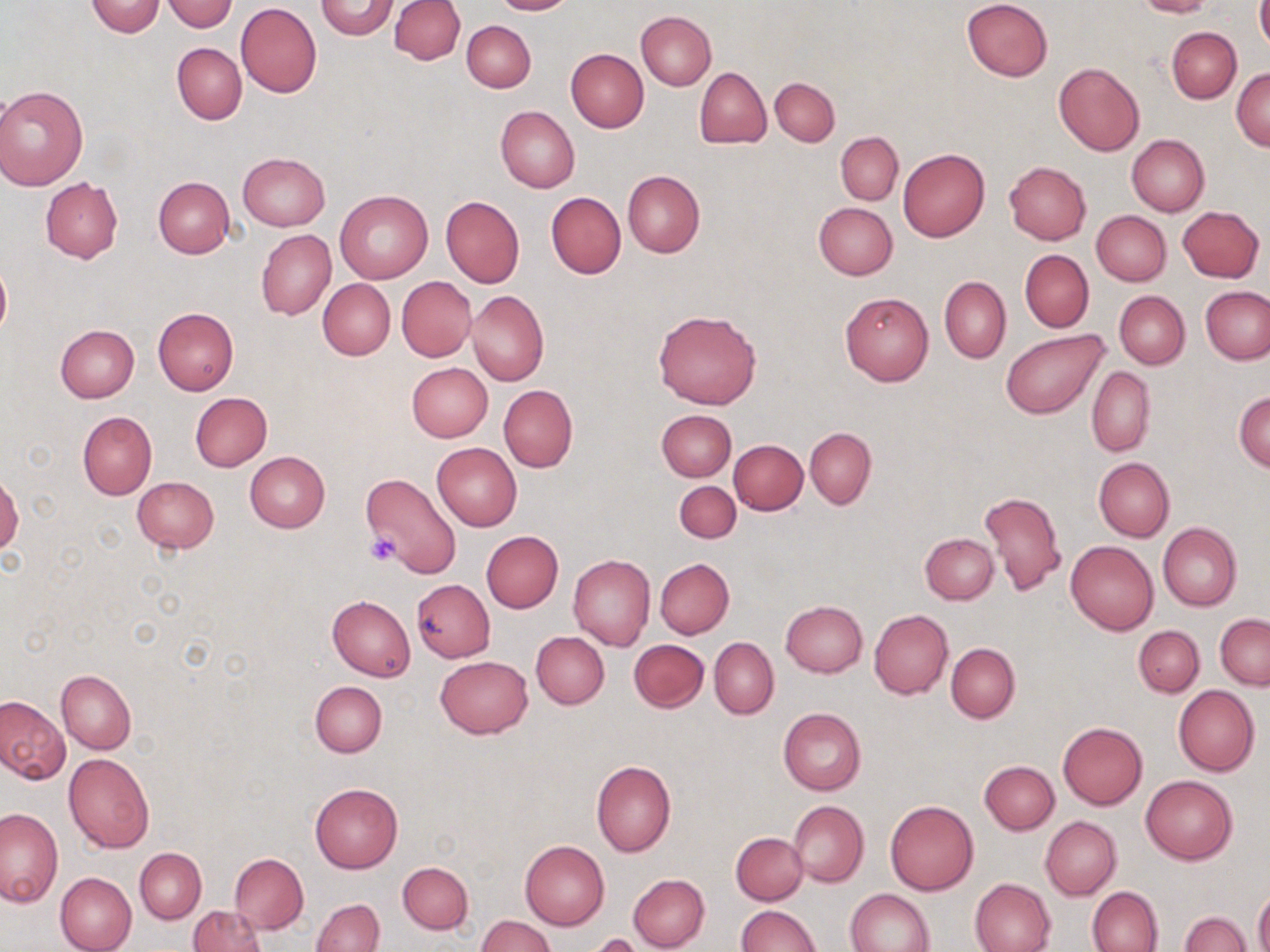

Summary:
  - Coordinate format: approximate bounding boxes as (x1,y1)-(x2,y2) corner pairs in pixels
  - Uninfected red blood cell locations: (84,0)-(166,37), (390,0)-(464,64), (490,0)-(577,15), (961,0)-(1053,82), (1134,0)-(1216,18), (1257,0)-(1270,54), (161,1)-(239,32), (315,1)-(399,39), (236,3)-(322,98), (637,11)-(716,90), (462,20)-(536,92), (1166,27)-(1240,104), (173,43)-(246,124), (565,49)-(649,132), (1053,61)-(1145,155), (1231,66)-(1270,150), (695,68)-(770,148), (769,76)-(839,147), (0,84)-(88,190), (495,106)-(579,193), (836,132)-(903,204), (834,135)-(972,214), (1126,135)-(1210,217), (898,148)-(989,242), (238,153)-(330,230), (1004,161)-(1091,244), (622,170)-(704,258), (154,177)-(235,258), (40,178)-(123,263), (335,189)-(432,283), (545,192)-(626,278), (441,195)-(524,287), (814,203)-(897,280), (1176,206)-(1263,282), (1090,210)-(1171,286), (256,229)-(336,319), (1020,249)-(1093,332), (0,256)-(11,344), (396,276)-(476,363), (940,276)-(1011,363), (318,278)-(395,359), (1200,286)-(1270,365), (466,289)-(549,386), (1114,291)-(1190,369), (839,292)-(934,385), (153,307)-(238,396), (652,309)-(762,410), (54,323)-(139,403), (1000,330)-(1108,419), (406,362)-(492,441), (1086,367)-(1155,456), (499,385)-(576,472), (1234,391)-(1270,471), (190,392)-(272,471), (656,409)-(735,481), (78,411)-(157,500), (805,428)-(876,508), (729,439)-(807,515), (432,442)-(521,531), (244,451)-(330,532), (1093,457)-(1174,542), (362,471)-(462,578), (0,472)-(21,559), (132,476)-(220,553), (675,480)-(741,542), (981,490)-(1067,598), (1157,522)-(1242,611), (482,531)-(563,612), (920,532)-(998,603), (1066,541)-(1158,634), (567,554)-(655,651), (655,559)-(734,638), (412,580)-(495,662), (327,595)-(415,681), (780,600)-(867,677), (869,609)-(953,699), (1216,614)-(1270,690), (1133,626)-(1204,697), (531,631)-(609,709), (709,638)-(778,719), (629,639)-(708,712), (946,642)-(1019,723), (435,655)-(533,738), (57,669)-(136,753), (311,681)-(387,757), (1173,686)-(1259,777), (0,696)-(69,783), (778,708)-(866,795), (1057,722)-(1147,809), (64,752)-(154,853), (591,760)-(676,857), (980,761)-(1059,834), (1141,776)-(1237,864), (310,782)-(403,873), (884,800)-(979,895), (789,801)-(868,887), (0,808)-(63,907), (1041,816)-(1121,901), (731,832)-(808,905), (520,840)-(610,929), (135,848)-(206,922), (230,852)-(308,934), (397,861)-(473,934), (55,872)-(138,952), (628,874)-(710,951), (970,878)-(1056,952), (1088,886)-(1163,952), (845,888)-(934,952), (1254,888)-(1270,952), (311,899)-(384,952), (188,905)-(266,952), (735,905)-(819,952), (1179,911)-(1251,951), (478,914)-(555,952), (585,934)-(644,952)
  - Platelet locations: (367,534)-(400,565)
  - Slide-level diagnosis: no evidence of blood parasites
  - Field of view: single
  - Modality: light microscopy
  - Magnification: 1000x
  - Preparation: thin blood film
  - Stain: May-Grünwald-Giemsa
  - Image size: 1270×952 pixels